Outline each blood parasite and name the species.
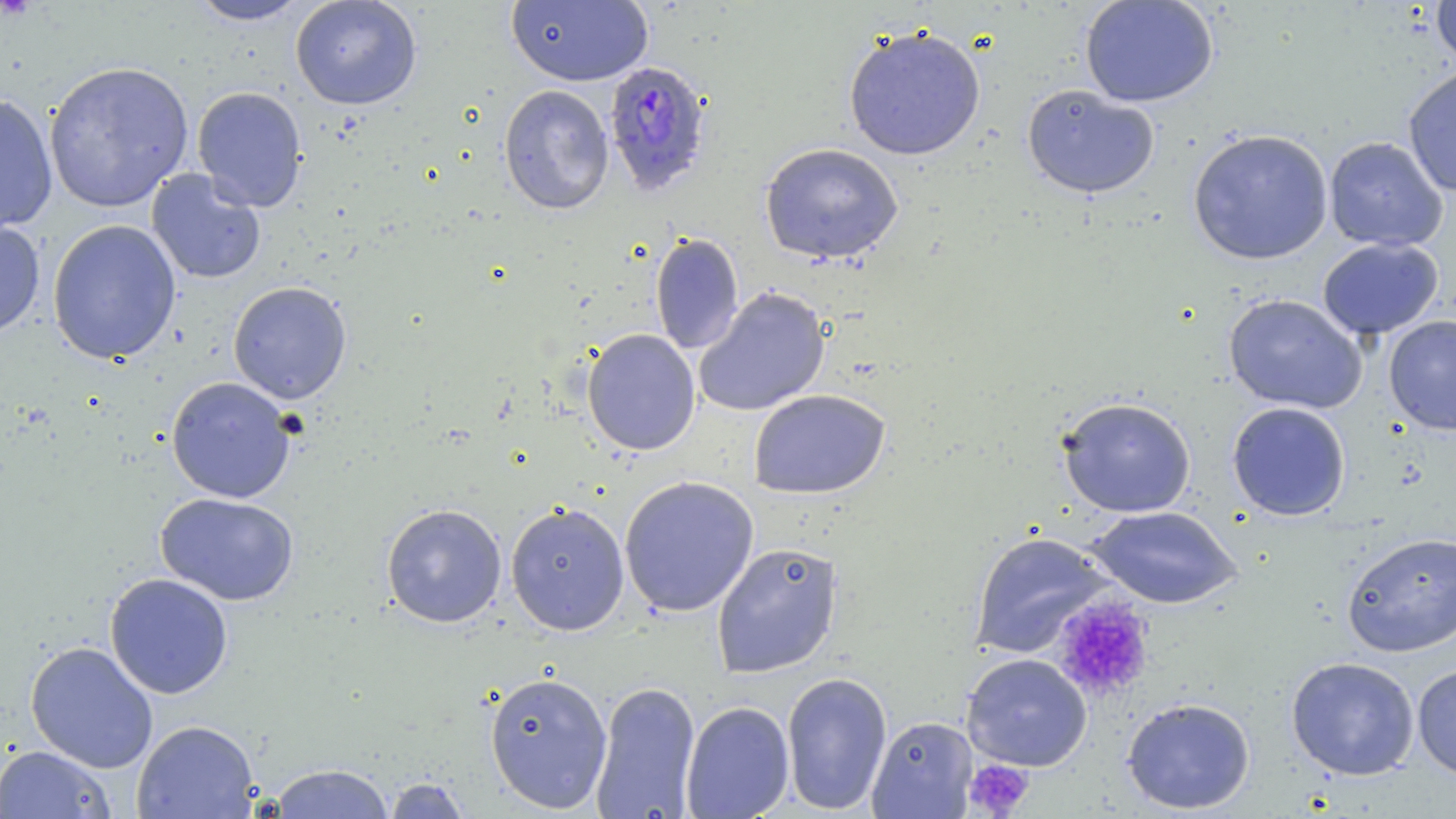
Approximate bounding boxes as (x1, y1, x2, y2) in pixels.
Plasmodium falciparum-infected red blood cells: (602, 60, 714, 196).
No Plasmodium ovale, Plasmodium malariae, Plasmodium vivax, Babesia divergens, or Trypanosoma brucei observed.

Summary:
  - Uninfected red blood cell locations: (185, 0, 313, 26), (290, 0, 422, 110), (505, 0, 654, 87), (1079, 0, 1219, 108), (1430, 0, 1456, 68), (843, 24, 987, 161), (43, 61, 194, 212), (1402, 67, 1456, 197), (498, 84, 615, 216), (1022, 84, 1160, 200), (192, 85, 308, 212), (0, 93, 59, 232), (1187, 128, 1333, 265), (1323, 136, 1448, 251), (760, 142, 904, 266), (145, 168, 267, 285), (0, 216, 46, 339), (46, 219, 182, 365), (650, 232, 744, 355), (1317, 237, 1444, 340), (228, 281, 352, 404), (693, 287, 831, 417), (1223, 293, 1367, 414), (1384, 315, 1456, 435), (582, 328, 701, 456), (166, 376, 298, 504), (749, 389, 891, 499), (1056, 396, 1197, 518), (1226, 401, 1351, 521), (618, 475, 760, 617), (155, 492, 300, 606), (505, 500, 630, 636), (381, 503, 507, 628), (1085, 506, 1242, 609), (968, 531, 1116, 659), (1341, 531, 1456, 657), (711, 541, 844, 678), (104, 573, 234, 699), (25, 641, 159, 773), (961, 653, 1092, 771), (1285, 656, 1420, 780), (1412, 663, 1456, 782), (781, 670, 892, 815), (484, 671, 613, 812), (590, 681, 701, 818), (1121, 696, 1256, 814), (680, 700, 795, 819), (867, 715, 978, 818), (132, 719, 259, 818), (0, 744, 116, 818), (267, 763, 396, 818), (382, 776, 473, 818)
  - Platelet locations: (1051, 597, 1155, 701), (964, 758, 1034, 817)
  - Slide-level diagnosis: Plasmodium falciparum
  - Stain: May-Grünwald-Giemsa
  - Image size: 1456×819 pixels
  - Preparation: thin blood smear
  - Magnification: 1000x
  - Modality: light microscopy
  - Field of view: single